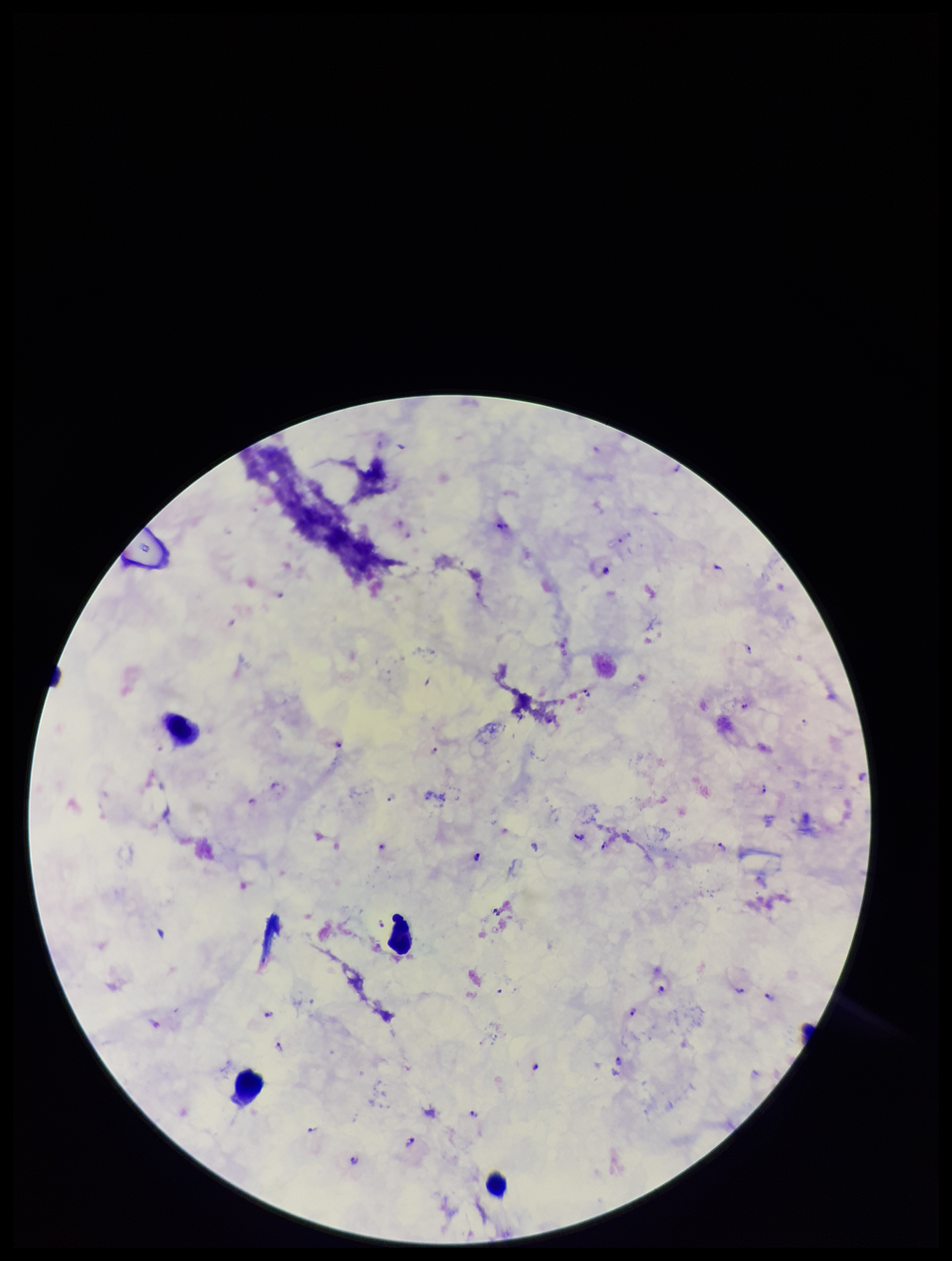
Species reported for this patient: Plasmodium falciparum. Patient malaria status: positive. Plasmodium parasites: seen. Leukocyte count: 4. Preparation: thick blood smear. Giemsa stain. Image is 952×1261 pixels. Photographed through the microscope eyepiece with a smartphone camera. One field from this slide. Parasite count: 22.